Mark where leukocytes are.
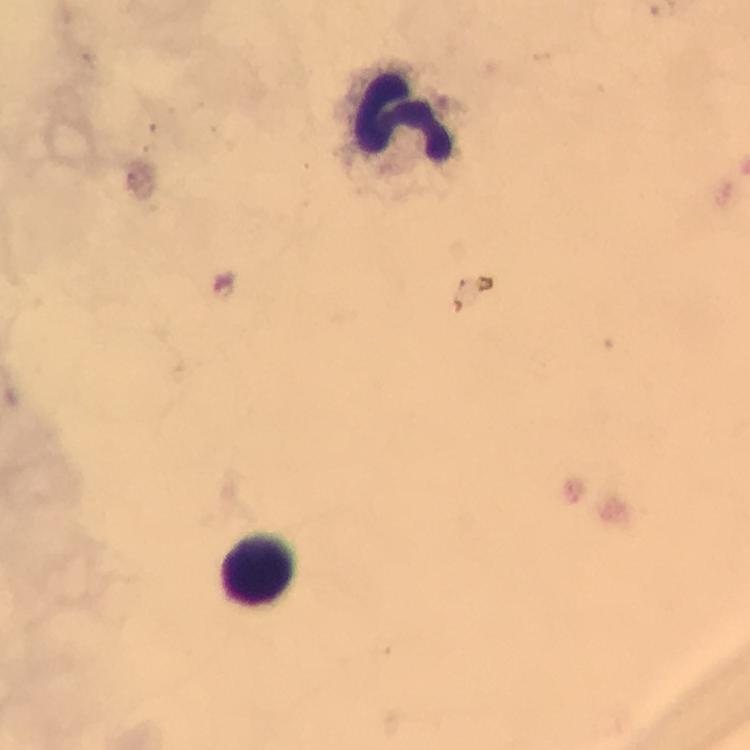

Approximate centers as [x, y] in pixels.
Leukocytes: [404, 121], [258, 569].

malaria parasites = none seen
capture = smartphone mounted on the microscope
magnification = 100x
context = from a malaria diagnostic workup
cropped from = one field of view
image size = 750×750 pixels
stain = Giemsa
preparation = thick blood film
immersion oil = applied